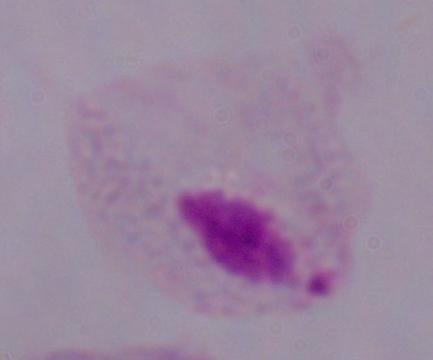
Micrograph. Captured at 1000x magnification. A trichomonad is shown.